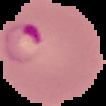
Summary:
  - Preparation: thin blood smear
  - Image type: cell region segmented out of the field of view; surrounding area masked to black
  - Image size: 106×106 pixels
  - Result: Plasmodium parasites identified